Classify this cell by malaria status.
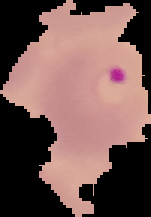

It is parasitized.

Image is 151×217 pixels. From a thin blood film. Cell region segmented out of the field of view; the surrounding area is masked to black.